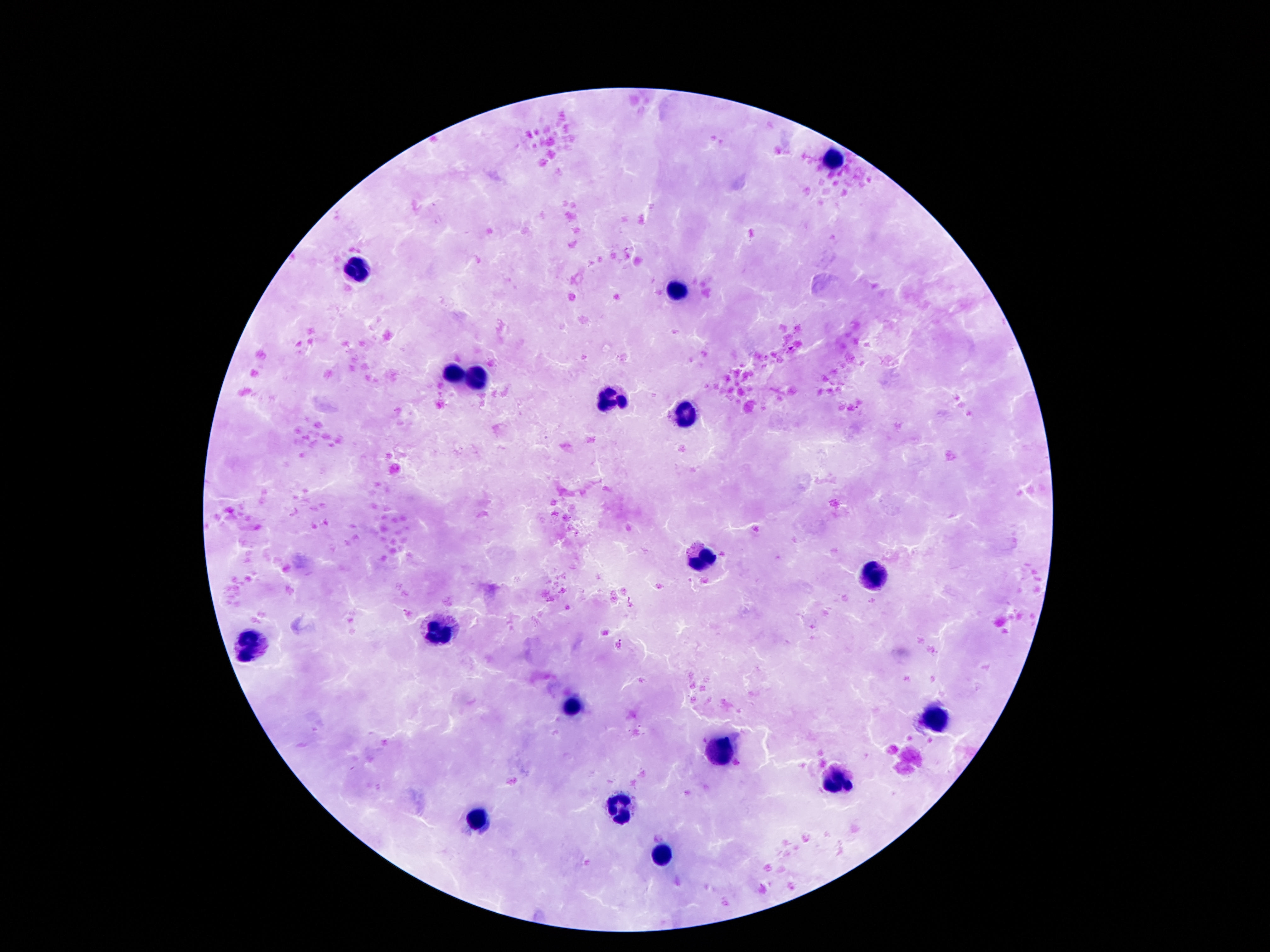
Approximate object centers, in pixels from the top-left corner.
Summary:
  - Leukocyte locations: (x=834, y=158), (x=360, y=272), (x=673, y=290), (x=453, y=374), (x=475, y=380), (x=607, y=399), (x=684, y=415), (x=700, y=558), (x=875, y=578), (x=434, y=632), (x=251, y=645), (x=573, y=706), (x=939, y=716), (x=730, y=746), (x=836, y=785), (x=616, y=806), (x=482, y=816), (x=662, y=860)
  - Stain: Giemsa
  - Image size: 1270×952 pixels
  - Preparation: thick peripheral-blood smear
  - Patient malaria status: not infected
  - Field of view: one from this slide
  - Capture: smartphone camera through the microscope eyepiece
  - Magnification: 100x